Name the parasite shown.
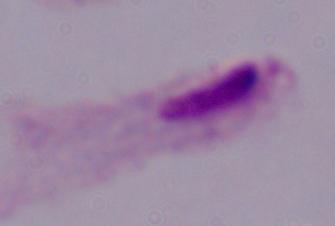
A trichomonad.

{
  "modality": "photomicrograph",
  "magnification": "1000x"
}